Report the malaria status of this cell.
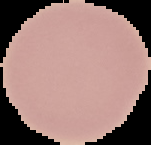
It is uninfected.

From a thin blood film. The area outside the segmented cell region is set to black. Image is 151×145 pixels.